Name the parasite shown.
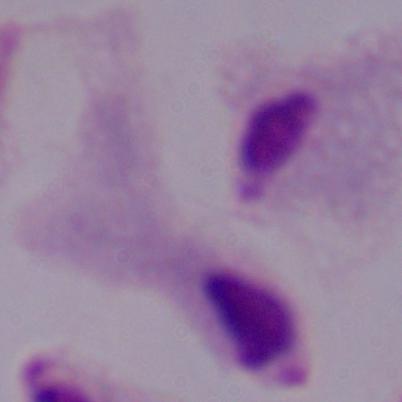

A trichomonad.

Summary:
  - Magnification: 1000x
  - Modality: photomicrograph